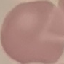

Summary:
  - Malaria status: uninfected
  - Image type: cell patch, automatically extracted from a larger field of view and resized to 64 × 64 pixels
  - Preparation: thin smear
  - Stain: Giemsa
  - Capture: smartphone camera at the microscope eyepiece